Point out each Plasmodium parasite and each leukocyte.
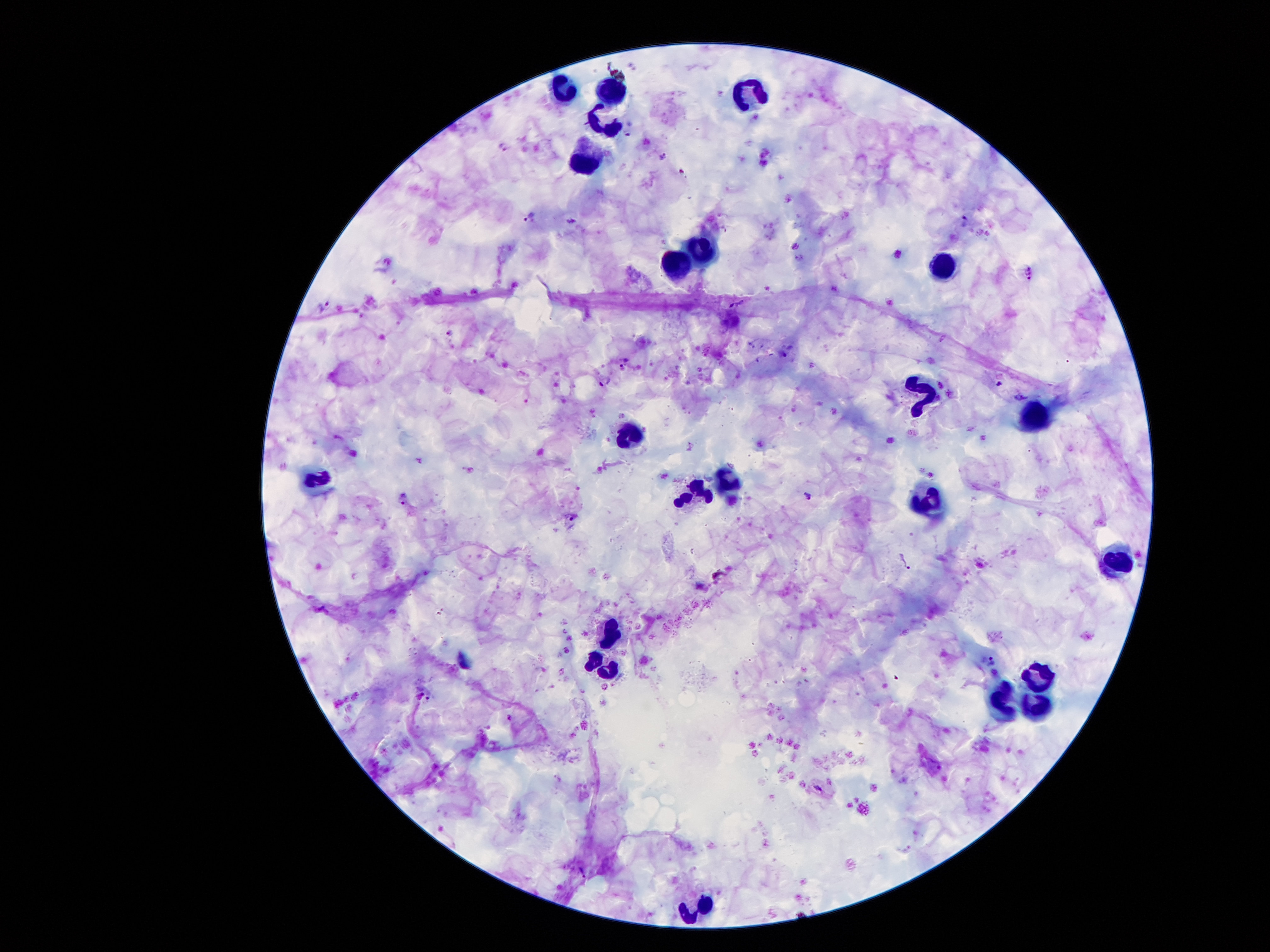

Approximate centers as (x, y) in pixels.
Plasmodium parasites: (505, 147), (662, 155), (530, 218), (966, 222), (1030, 274), (327, 309), (450, 333), (605, 381), (808, 495), (403, 498), (573, 516), (992, 661), (818, 789), (582, 871).
Leukocytes: (607, 90), (563, 92), (744, 92), (603, 124), (584, 156), (704, 250), (937, 267), (676, 269), (910, 397), (1029, 416), (622, 443), (725, 479), (311, 483), (693, 496), (930, 507), (1115, 565), (607, 633), (1042, 668), (599, 675), (1000, 702), (1036, 702), (697, 902).

field of view = one from this slide
stain = Giemsa
patient malaria status = infected with Plasmodium falciparum
capture = smartphone through the microscope eyepiece
image size = 1270×952 pixels
preparation = thick blood smear
magnification = 100x